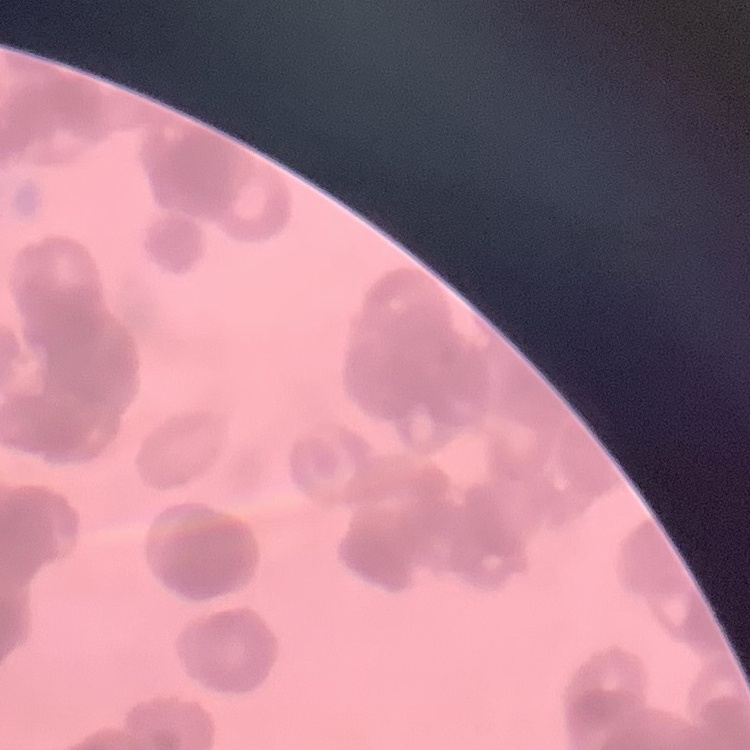
erythrocyte_morphology: rouleaux formation
stain: Field's or Giemsa
image_type: square crop of a larger photomicrograph
preparation: thin peripheral smear